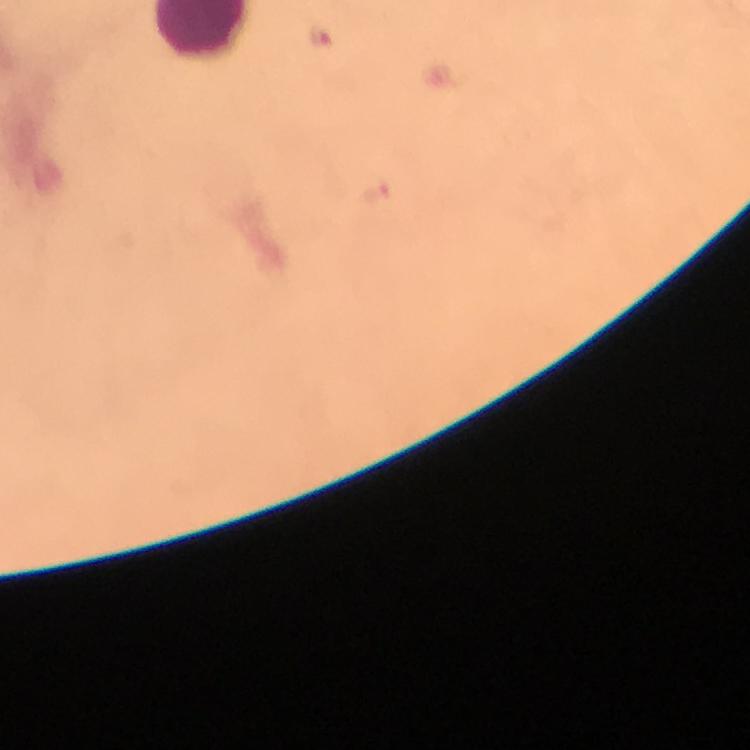

Approximate centers as (x, y) in pixels. Plasmodium parasite locations: (322, 39). 100x magnification. Photographed through the microscope with a smartphone camera. Thick blood film. From a malaria diagnostic workup. Immersion oil was used. Image is 750×750 pixels. A crop from one field of view. Giemsa-stained preparation.